Name the cell type shown.
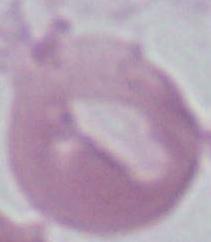

This is an erythrocyte.

Summary:
  - Modality: micrograph
  - Magnification: 1000x